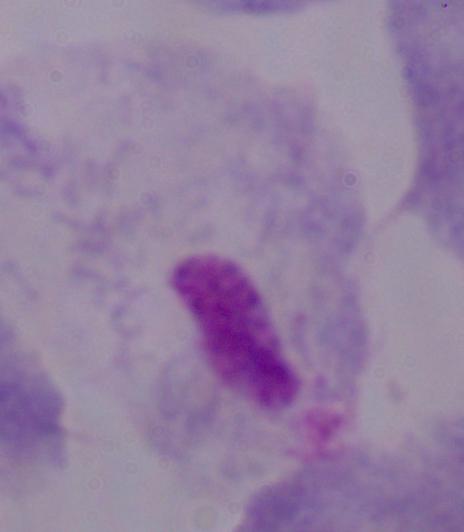
{
  "modality": "micrograph",
  "magnification": "1000x",
  "identification": "trichomonad"
}